Locate and identify every blood parasite.
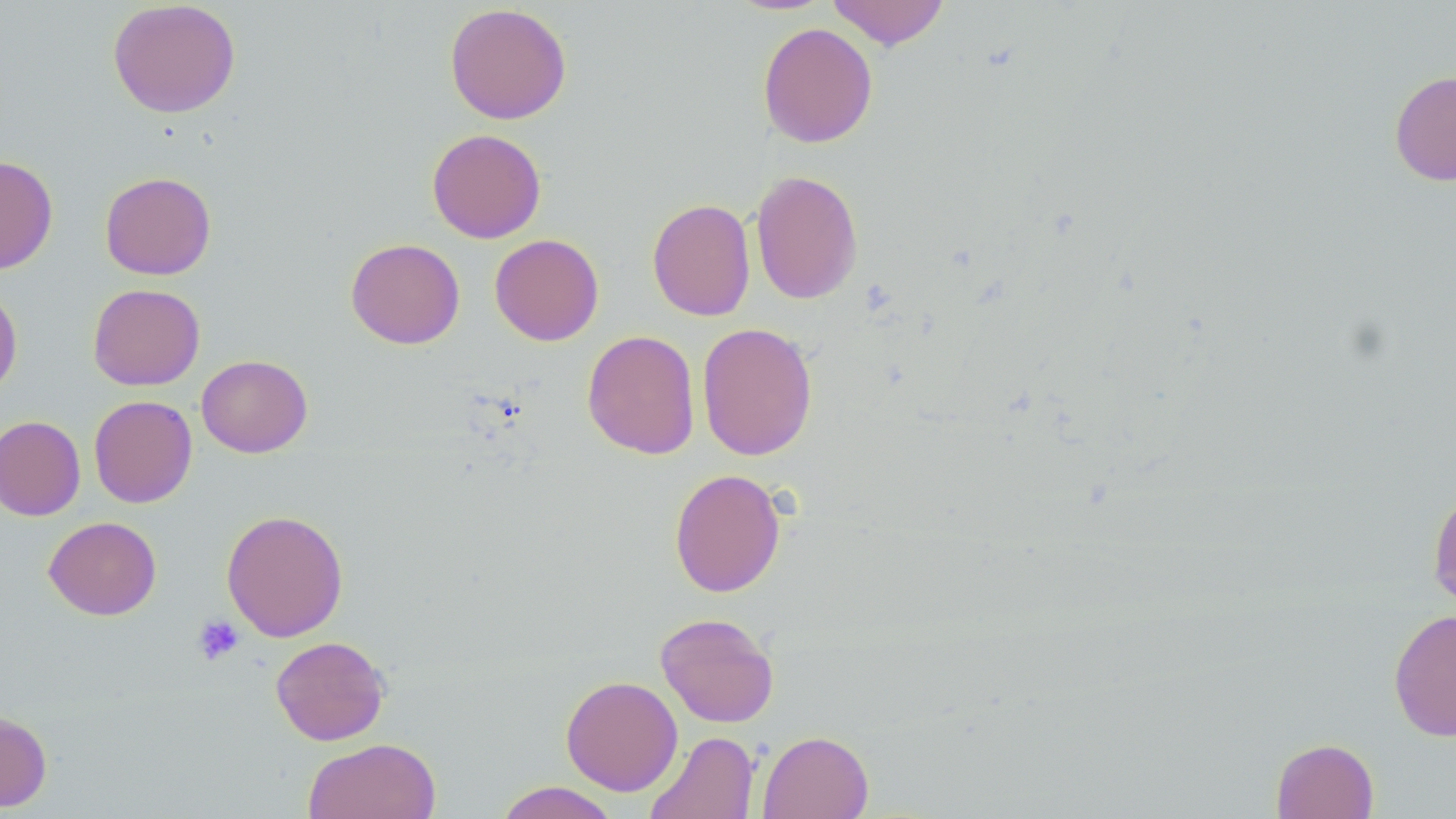
No blood parasites observed.

slide-level diagnosis = no evidence of blood parasites
modality = light microscopy
preparation = thin blood film
image size = 1456×819 pixels
platelet locations = approximate bounding boxes as named x1/y1/x2/y2 corners in pixels: (x1=192, y1=614, x2=245, y2=666)
uninfected red blood cell locations = approximate bounding boxes as named x1/y1/x2/y2 corners in pixels: (x1=826, y1=0, x2=950, y2=50), (x1=107, y1=1, x2=241, y2=118), (x1=444, y1=3, x2=572, y2=125), (x1=757, y1=22, x2=878, y2=148), (x1=1389, y1=70, x2=1456, y2=186), (x1=426, y1=128, x2=546, y2=243), (x1=0, y1=155, x2=58, y2=274), (x1=751, y1=169, x2=864, y2=305), (x1=100, y1=171, x2=216, y2=279), (x1=647, y1=198, x2=756, y2=321), (x1=489, y1=234, x2=604, y2=346), (x1=346, y1=238, x2=465, y2=349), (x1=0, y1=283, x2=23, y2=399), (x1=88, y1=283, x2=205, y2=390), (x1=697, y1=322, x2=818, y2=461), (x1=582, y1=330, x2=700, y2=460), (x1=196, y1=354, x2=313, y2=458), (x1=89, y1=395, x2=197, y2=508), (x1=0, y1=415, x2=85, y2=521), (x1=669, y1=468, x2=786, y2=598), (x1=1427, y1=483, x2=1456, y2=613), (x1=221, y1=509, x2=348, y2=641), (x1=44, y1=516, x2=161, y2=620), (x1=1388, y1=608, x2=1456, y2=742), (x1=655, y1=611, x2=780, y2=727), (x1=270, y1=635, x2=391, y2=745), (x1=560, y1=675, x2=683, y2=796), (x1=0, y1=710, x2=52, y2=812), (x1=645, y1=730, x2=759, y2=819), (x1=758, y1=730, x2=873, y2=819), (x1=1271, y1=737, x2=1379, y2=819), (x1=303, y1=738, x2=441, y2=819), (x1=493, y1=781, x2=621, y2=819)
field of view = single
stain = May-Grünwald-Giemsa
magnification = 1000x